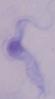 A trypanosome is seen. Micrograph. Captured at 1000x magnification.